Give the extent of all uninfected red blood cells.
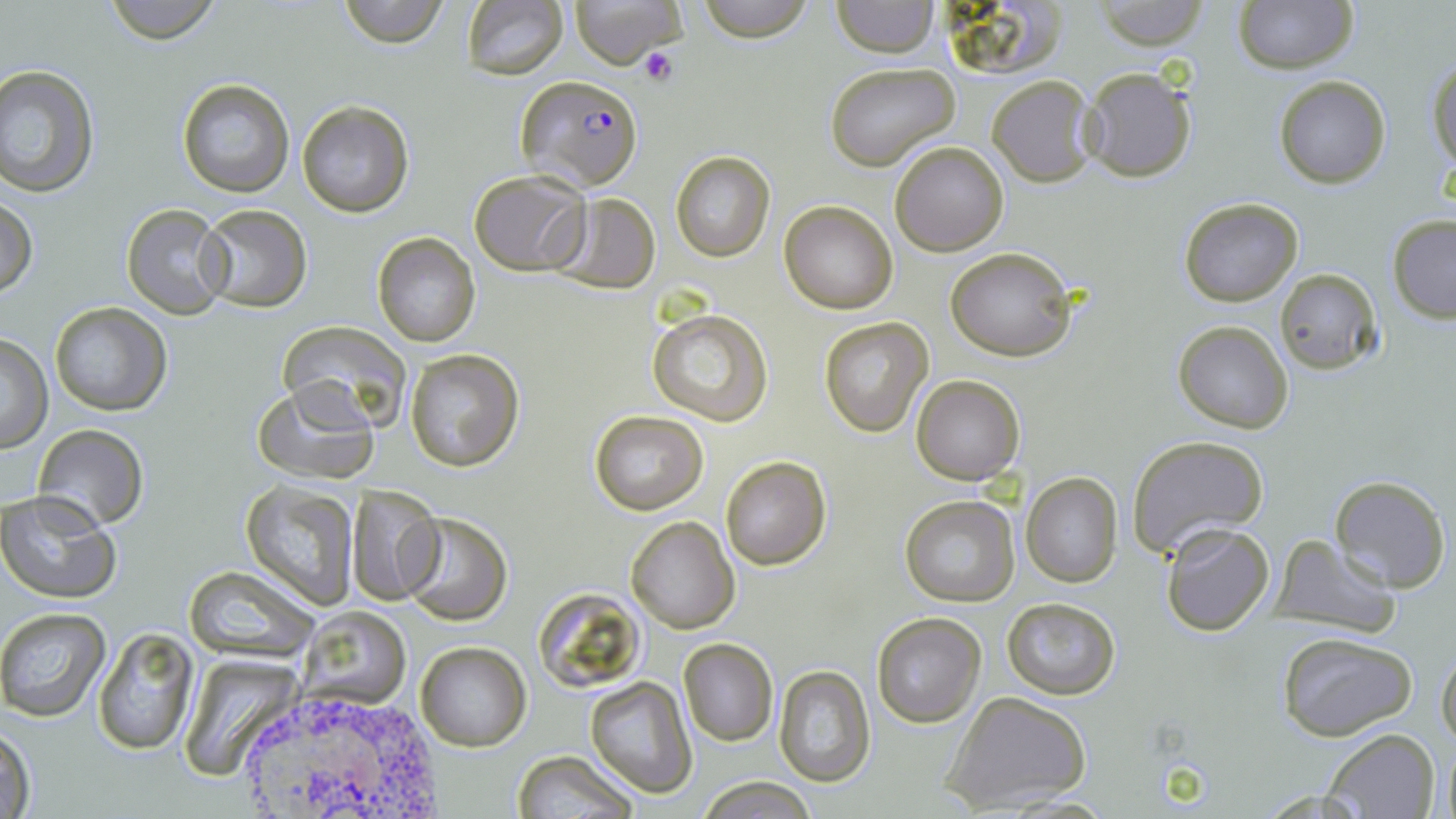

Approximate bounding boxes as named x1/y1/x2/y2 corners in pixels.
Uninfected red blood cells: (x1=100, y1=0, x2=225, y2=44), (x1=335, y1=0, x2=453, y2=47), (x1=460, y1=0, x2=570, y2=81), (x1=569, y1=0, x2=686, y2=70), (x1=692, y1=0, x2=817, y2=42), (x1=1095, y1=0, x2=1208, y2=49), (x1=1234, y1=0, x2=1356, y2=72), (x1=830, y1=1, x2=939, y2=57), (x1=939, y1=1, x2=1063, y2=80), (x1=1428, y1=59, x2=1455, y2=170), (x1=824, y1=62, x2=960, y2=172), (x1=0, y1=64, x2=99, y2=195), (x1=1079, y1=65, x2=1199, y2=183), (x1=987, y1=75, x2=1097, y2=187), (x1=1273, y1=75, x2=1392, y2=188), (x1=177, y1=78, x2=295, y2=198), (x1=297, y1=101, x2=414, y2=218), (x1=890, y1=141, x2=1009, y2=256), (x1=670, y1=150, x2=776, y2=262), (x1=468, y1=171, x2=590, y2=275), (x1=548, y1=193, x2=662, y2=294), (x1=1, y1=196, x2=37, y2=300), (x1=1180, y1=197, x2=1303, y2=307), (x1=780, y1=202, x2=897, y2=313), (x1=121, y1=203, x2=230, y2=320), (x1=196, y1=204, x2=311, y2=312), (x1=1386, y1=214, x2=1456, y2=322), (x1=372, y1=232, x2=481, y2=348), (x1=946, y1=247, x2=1077, y2=362), (x1=1275, y1=268, x2=1382, y2=374), (x1=50, y1=302, x2=171, y2=415), (x1=648, y1=309, x2=774, y2=426), (x1=817, y1=317, x2=933, y2=437), (x1=1173, y1=320, x2=1294, y2=433), (x1=279, y1=322, x2=412, y2=431), (x1=0, y1=336, x2=54, y2=454), (x1=405, y1=350, x2=525, y2=472), (x1=912, y1=374, x2=1025, y2=485), (x1=253, y1=379, x2=381, y2=485), (x1=589, y1=410, x2=709, y2=514), (x1=33, y1=424, x2=148, y2=530), (x1=1127, y1=434, x2=1269, y2=558), (x1=721, y1=456, x2=830, y2=569), (x1=1020, y1=472, x2=1124, y2=588), (x1=1329, y1=474, x2=1452, y2=592), (x1=241, y1=481, x2=359, y2=609), (x1=345, y1=483, x2=442, y2=604), (x1=0, y1=490, x2=120, y2=604), (x1=898, y1=495, x2=1020, y2=607), (x1=398, y1=512, x2=511, y2=624), (x1=626, y1=515, x2=741, y2=635), (x1=1158, y1=520, x2=1276, y2=637), (x1=1271, y1=536, x2=1403, y2=638), (x1=183, y1=566, x2=318, y2=658), (x1=533, y1=585, x2=651, y2=694), (x1=1000, y1=596, x2=1122, y2=699), (x1=0, y1=608, x2=111, y2=720), (x1=302, y1=608, x2=409, y2=708), (x1=871, y1=611, x2=988, y2=729), (x1=92, y1=624, x2=199, y2=755), (x1=1275, y1=631, x2=1418, y2=742), (x1=679, y1=640, x2=778, y2=746), (x1=1437, y1=640, x2=1456, y2=754), (x1=415, y1=642, x2=530, y2=750), (x1=180, y1=658, x2=311, y2=778), (x1=772, y1=666, x2=876, y2=786), (x1=585, y1=677, x2=697, y2=797), (x1=941, y1=693, x2=1093, y2=813), (x1=2, y1=717, x2=37, y2=819), (x1=1317, y1=729, x2=1441, y2=818), (x1=510, y1=751, x2=639, y2=819), (x1=696, y1=776, x2=816, y2=817).

{
  "slide_level_diagnosis": "Plasmodium falciparum",
  "stain": "May-Grünwald-Giemsa",
  "image_size": "1456×819 pixels",
  "preparation": "thin blood smear",
  "magnification": "1000x",
  "plasmodium_falciparum_infected_red_blood_cell_locations": "approximate bounding boxes as named x1/y1/x2/y2 corners in pixels: (x1=514, y1=74, x2=645, y2=189)",
  "white_blood_cell_locations": "approximate bounding boxes as named x1/y1/x2/y2 corners in pixels: (x1=226, y1=677, x2=446, y2=819)",
  "platelet_locations": "approximate bounding boxes as named x1/y1/x2/y2 corners in pixels: (x1=638, y1=45, x2=680, y2=87)",
  "field_of_view": "one of a larger specimen",
  "modality": "light microscopy"
}